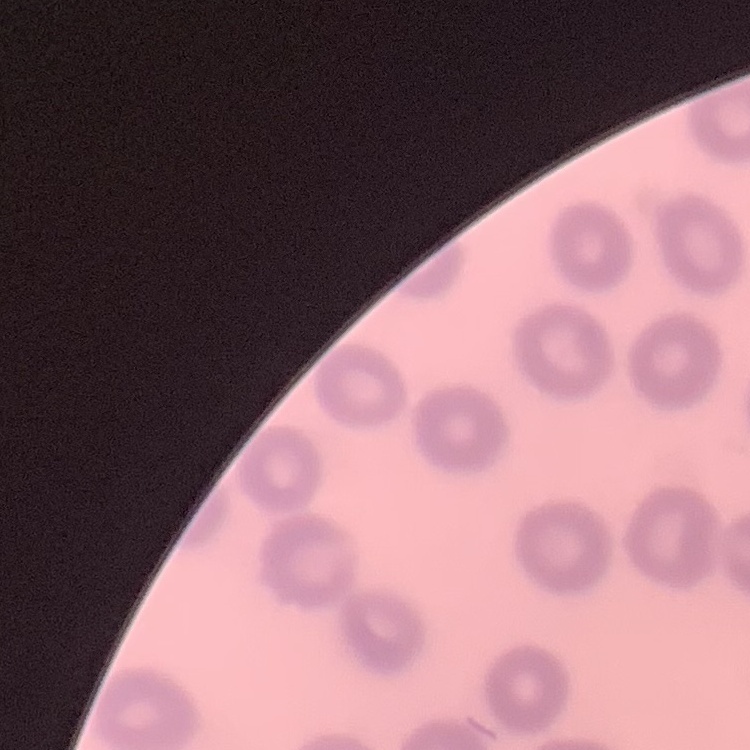

{
  "red_blood_cell_morphology": "no rouleaux formation",
  "image_type": "square crop of a larger photomicrograph",
  "stain": "Field's or Giemsa",
  "preparation": "thin blood smear"
}